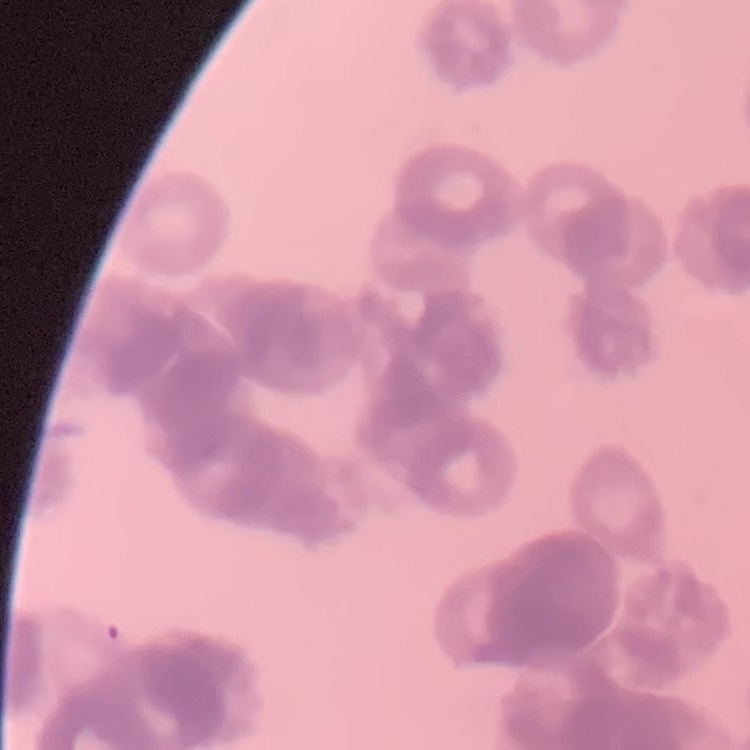
{
  "red_blood_cell_morphology": "rouleaux formation",
  "preparation": "thin blood film",
  "image_type": "one tile cut from a larger photomicrograph",
  "stain": "Field's or Giemsa"
}